Report the malaria status of this cell.
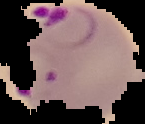

Parasitized.

Image is 145×124 pixels. From a thin blood film. Segmented cell region on a black background.